Point out leukocytes.
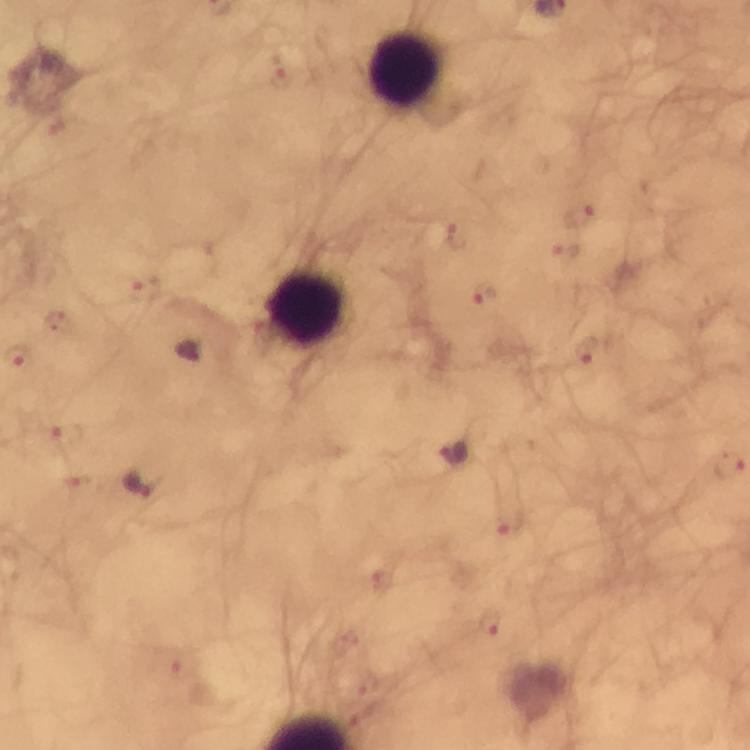

Approximate centers as [x, y] in pixels.
Leukocytes: [404, 68], [305, 307].

Malaria parasite locations: [283, 78], [580, 216], [458, 235], [565, 252], [144, 289], [484, 293], [56, 324], [586, 351], [68, 435], [454, 453], [730, 466], [140, 484], [508, 522], [490, 621], [173, 663]. 100x magnification. From a malaria diagnostic workup. Immersion oil applied. Thick smear. Photographed through the microscope with a smartphone camera. Giemsa-stained preparation. Image is 750×750 pixels. A crop from one field of view.